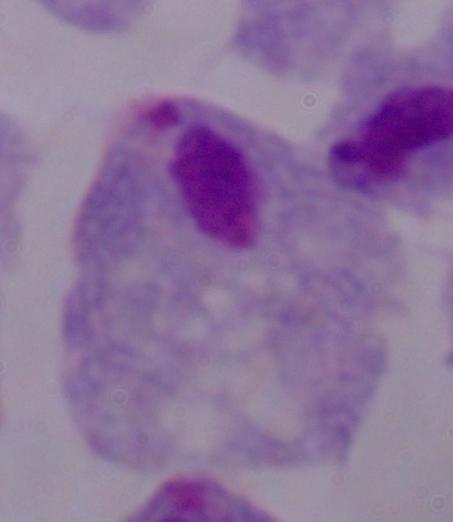

A trichomonad is shown. Micrograph. 1000x magnification.